Give the position of every Plasmodium parasite.
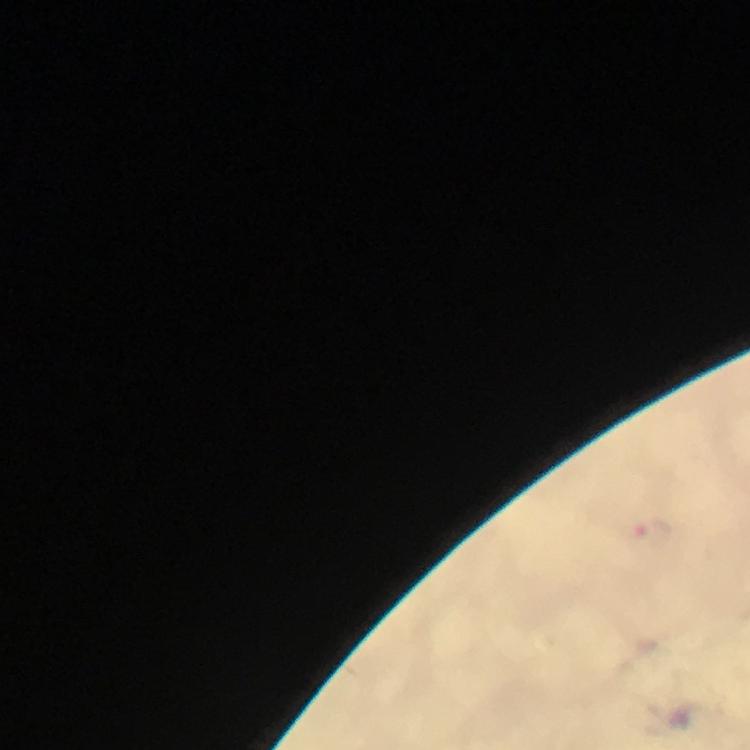

Approximate centers as {x, y} in pixels.
Plasmodium parasites: {653, 528}.

100x magnification. From a malaria diagnostic workup. Immersion oil was used. Image is 750×750 pixels. Smartphone photograph taken through a microscope. A crop from one field of view. Giemsa stain. Thick blood film.